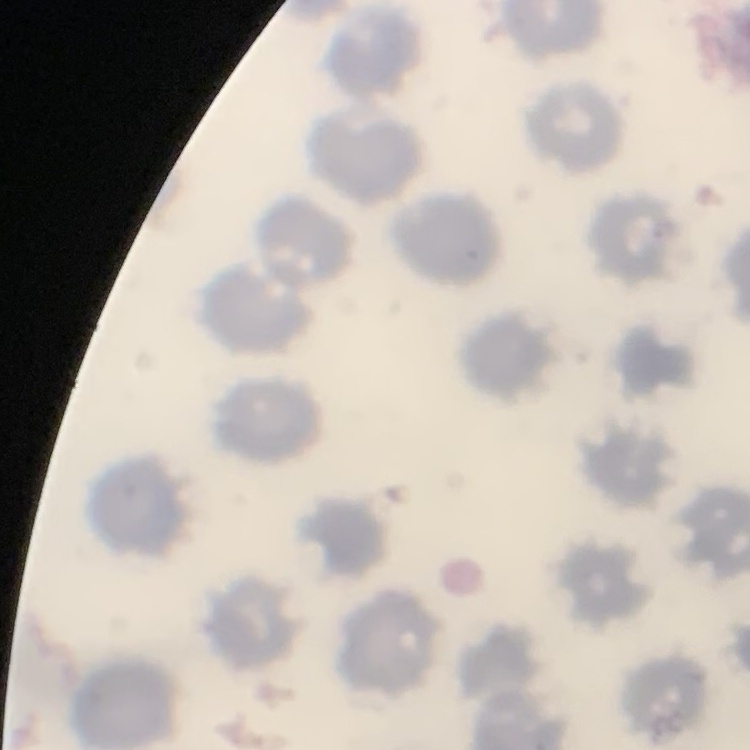 The red blood cells exhibit no rouleaux formation. One tile cut from a larger photomicrograph. Thin blood film. Field's or Giemsa stain.